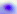
modality = photomicrograph
magnification = 400x
identification = Toxoplasma gondii